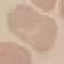
Summary:
  - Malaria status: uninfected
  - Capture: smartphone camera at the microscope eyepiece
  - Stain: Giemsa
  - Image type: automatically extracted cell patch, resized to 64 × 64 pixels
  - Preparation: thin smear